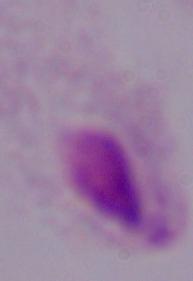

Summary:
  - Magnification: 1000x
  - Identification: trichomonad
  - Modality: micrograph